Locate every uninfected red blood cell.
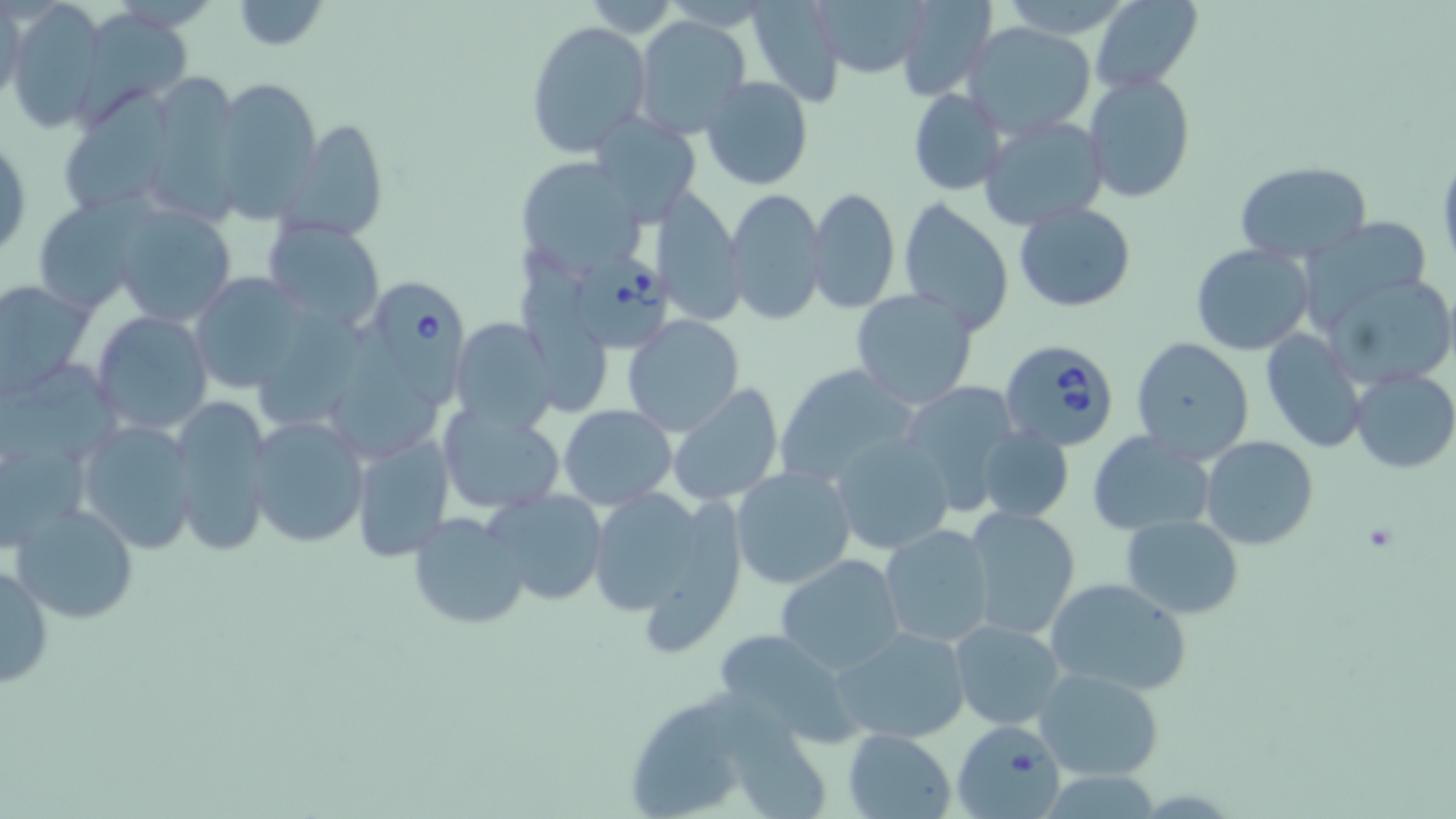

Approximate bounding boxes as (x1,y1)-(x2,y2) corner pairs in pixels.
Uninfected red blood cells: (229,0)-(328,51), (581,0)-(678,34), (746,0)-(846,108), (896,0)-(995,101), (997,0)-(1136,39), (1089,0)-(1202,92), (1,1)-(24,113), (5,2)-(107,129), (79,9)-(191,115), (633,14)-(751,141), (524,19)-(651,157), (962,20)-(1098,137), (1082,73)-(1195,205), (210,76)-(322,221), (700,76)-(814,190), (908,89)-(1006,194), (590,112)-(699,226), (976,113)-(1111,233), (284,120)-(391,242), (1,132)-(30,265), (1435,150)-(1456,271), (523,159)-(641,268), (1234,160)-(1371,265), (653,186)-(745,325), (725,187)-(826,326), (806,187)-(899,315), (34,198)-(151,310), (898,198)-(1014,333), (1014,201)-(1138,312), (111,204)-(239,328), (1299,217)-(1435,321), (262,218)-(385,332), (1190,244)-(1315,354), (1321,271)-(1456,391), (187,272)-(313,395), (0,279)-(92,398), (849,289)-(981,410), (90,311)-(214,436), (622,313)-(745,436), (450,318)-(557,436), (1262,329)-(1367,451), (1130,336)-(1254,464), (771,362)-(919,489), (1349,368)-(1456,474), (895,379)-(1027,515), (665,381)-(787,508), (170,395)-(274,555), (557,404)-(677,511), (436,405)-(565,516), (246,415)-(370,547), (73,419)-(199,554), (977,429)-(1074,523), (348,432)-(454,562), (1086,432)-(1214,535), (829,433)-(956,558), (0,434)-(88,553), (1200,436)-(1319,552), (731,466)-(855,590), (586,486)-(734,630), (484,488)-(609,605), (964,504)-(1083,641), (11,505)-(137,624), (405,510)-(530,632), (1121,515)-(1245,619), (879,524)-(995,649), (774,554)-(906,674), (0,561)-(51,690), (1043,576)-(1192,699), (949,618)-(1067,730), (832,626)-(971,745), (713,627)-(855,744), (1034,667)-(1165,781), (952,718)-(1066,818), (841,729)-(955,819).

Babesia divergens-infected red blood cell locations = approximate bounding boxes as (x1,y1)-(x2,y2) corner pairs in pixels: (561,246)-(672,346), (369,275)-(475,416), (999,340)-(1122,454)
slide-level diagnosis = Babesia divergens
stain = May-Grünwald-Giemsa
field of view = one of a larger specimen
image size = 1456×819 pixels
magnification = 1000x
preparation = thin blood film
modality = optical microscopy